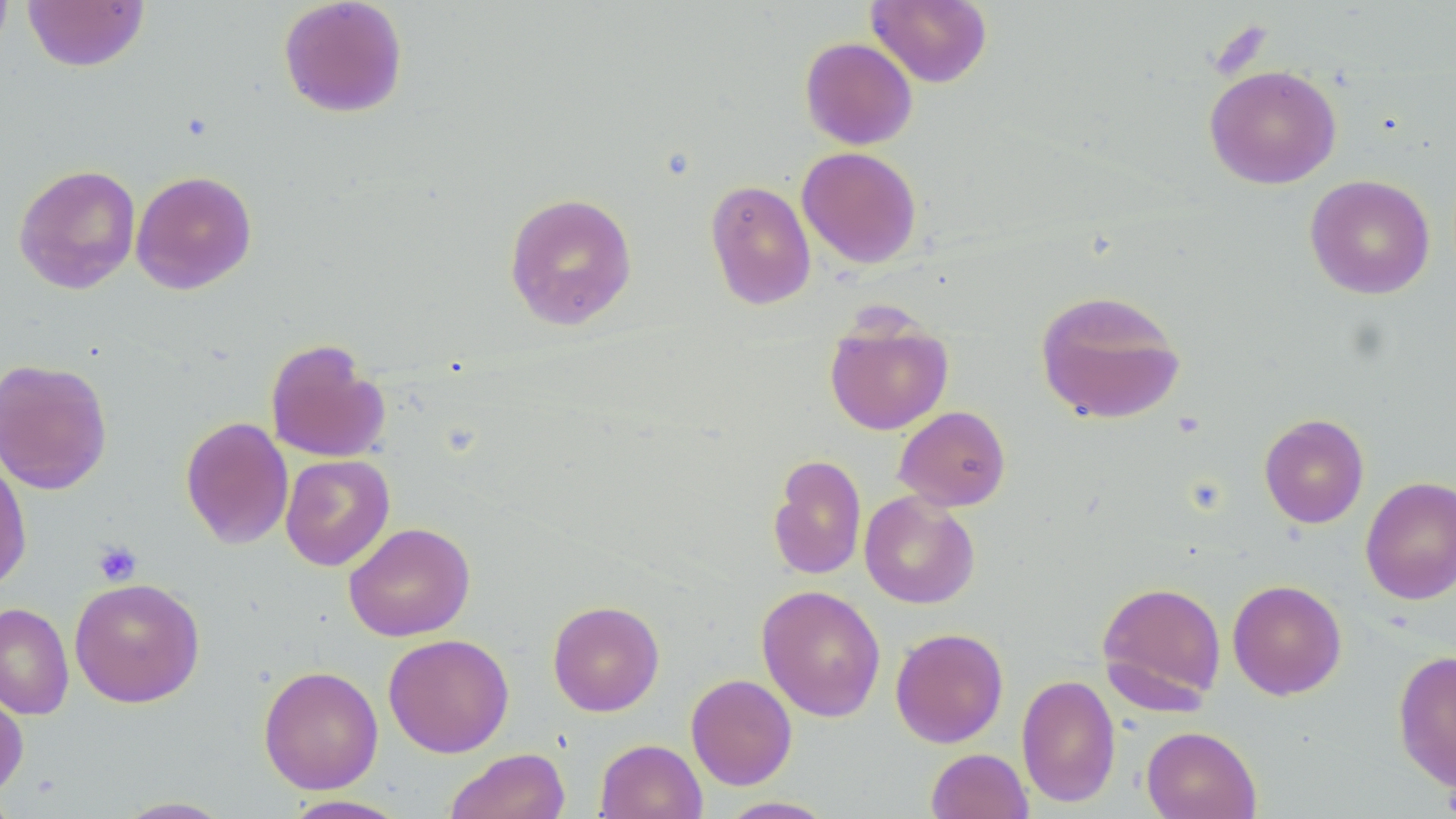
slide-level diagnosis = negative for blood parasites
field of view = one of a larger specimen
uninfected red blood cell locations = approximate bounding boxes as [x1, y1, x2, y2] in pixels: [0, 0, 14, 58], [22, 0, 150, 72], [278, 0, 408, 119], [867, 0, 992, 88], [800, 37, 918, 150], [1204, 65, 1342, 189], [797, 146, 922, 269], [14, 163, 141, 294], [131, 170, 257, 295], [1304, 174, 1436, 299], [704, 179, 817, 310], [504, 191, 638, 331], [1034, 289, 1186, 425], [824, 313, 953, 435], [265, 339, 390, 463], [0, 357, 113, 495], [894, 405, 1011, 511], [1259, 413, 1369, 528], [180, 416, 294, 550], [280, 454, 395, 571], [768, 454, 866, 581], [0, 455, 32, 593], [1360, 476, 1456, 605], [859, 491, 980, 609], [343, 522, 475, 642], [69, 577, 205, 707], [1227, 579, 1347, 699], [1096, 580, 1227, 709], [756, 584, 886, 721], [547, 600, 665, 716], [0, 602, 74, 720], [890, 627, 1009, 748], [383, 633, 514, 758], [1392, 650, 1456, 792], [258, 664, 384, 795], [686, 673, 797, 790], [1016, 674, 1120, 807], [0, 687, 28, 800], [1141, 725, 1261, 819], [595, 738, 707, 819], [443, 748, 571, 819], [926, 748, 1033, 819], [281, 795, 410, 818], [112, 796, 236, 818], [716, 796, 839, 818]
magnification = 1000x
modality = light microscopy
preparation = thin blood smear
stain = May-Grünwald-Giemsa
image size = 1456×819 pixels
platelet locations = approximate bounding boxes as [x1, y1, x2, y2] in pixels: [93, 541, 141, 586], [1442, 783, 1456, 816]